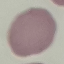

result: no malaria parasites seen
stain: Giemsa
preparation: thin smear
capture: smartphone camera at the microscope eyepiece
image_type: cell patch, automatically extracted from a larger field of view and resized to 64 × 64 pixels